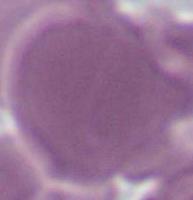
{
  "modality": "micrograph",
  "identification": "erythrocyte",
  "magnification": "1000x"
}